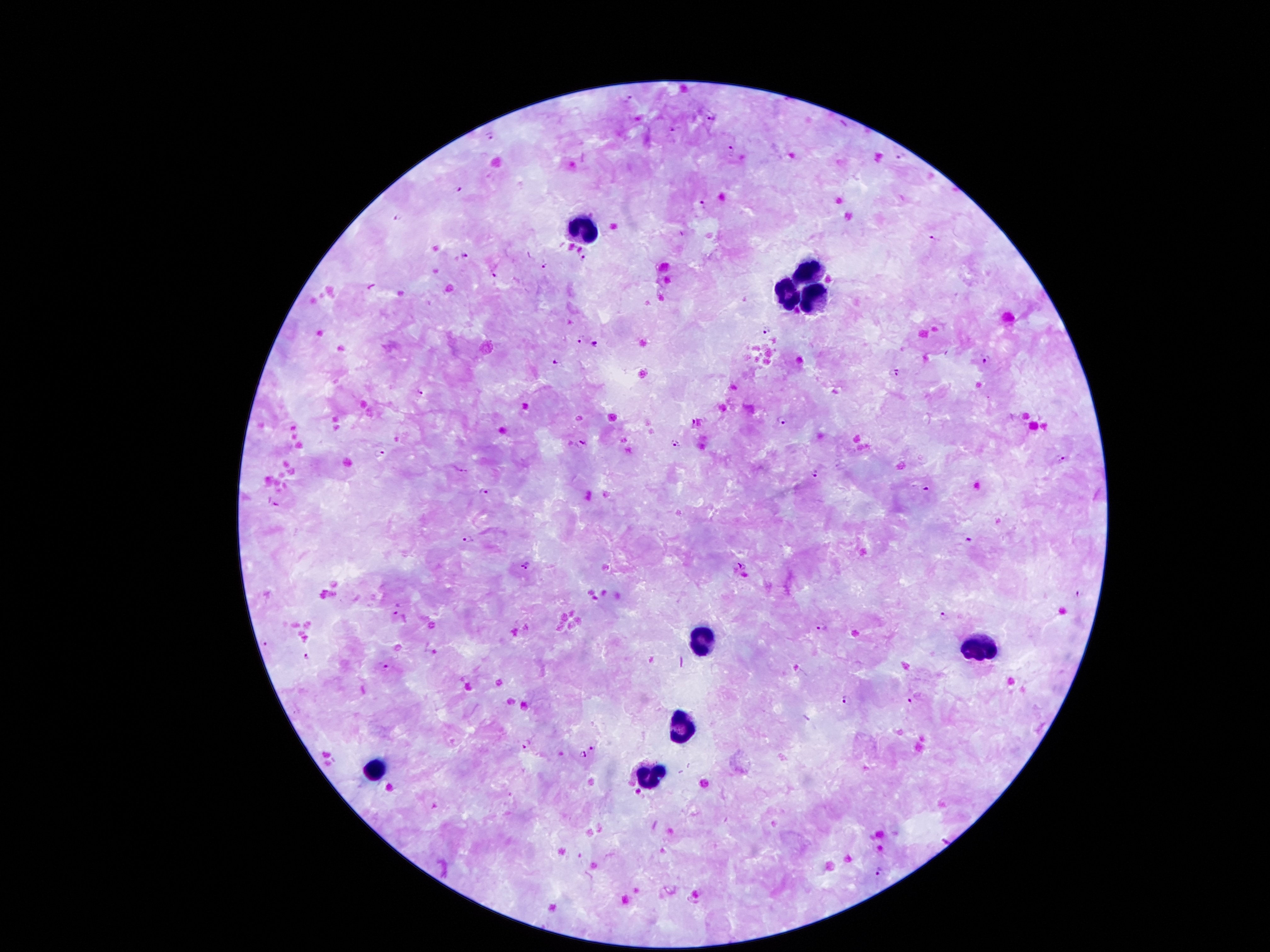
Approximate object centers, in pixels from the top-left corner. Leukocyte locations: (x=582, y=227), (x=807, y=270), (x=783, y=292), (x=813, y=295), (x=699, y=641), (x=978, y=647), (x=685, y=723), (x=376, y=766), (x=653, y=774). Malaria parasite locations: (x=629, y=95), (x=711, y=115), (x=674, y=128), (x=491, y=133), (x=730, y=150), (x=900, y=156), (x=458, y=188), (x=703, y=206), (x=397, y=215), (x=933, y=239), (x=463, y=254), (x=583, y=257), (x=545, y=266), (x=492, y=274), (x=768, y=329), (x=579, y=339), (x=595, y=345), (x=987, y=358), (x=556, y=361), (x=896, y=374), (x=419, y=391), (x=783, y=420), (x=583, y=444), (x=675, y=444), (x=381, y=455), (x=1061, y=458), (x=816, y=473), (x=926, y=488), (x=484, y=491), (x=275, y=503), (x=470, y=539), (x=969, y=540), (x=527, y=565), (x=741, y=566), (x=1079, y=594), (x=399, y=608), (x=944, y=613), (x=823, y=627), (x=266, y=643), (x=306, y=656), (x=383, y=665), (x=846, y=698), (x=910, y=698), (x=528, y=744), (x=591, y=748), (x=582, y=755), (x=945, y=840), (x=881, y=869). One field from this slide. 100x magnification. Thick peripheral-blood smear. Image is 1270×952 pixels. Giemsa stain. Patient malaria status: infected with Plasmodium falciparum. Smartphone photograph taken through the microscope eyepiece.